Describe the morphology of the erythrocytes.
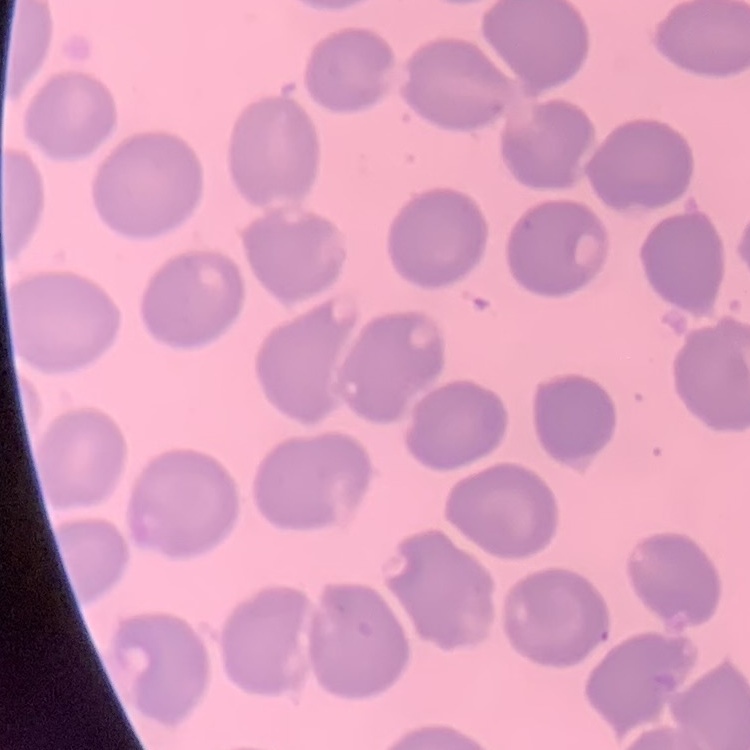

No rouleaux formation.

Stained with either Field's or Giemsa. Thin blood smear. Square crop of a larger photomicrograph.